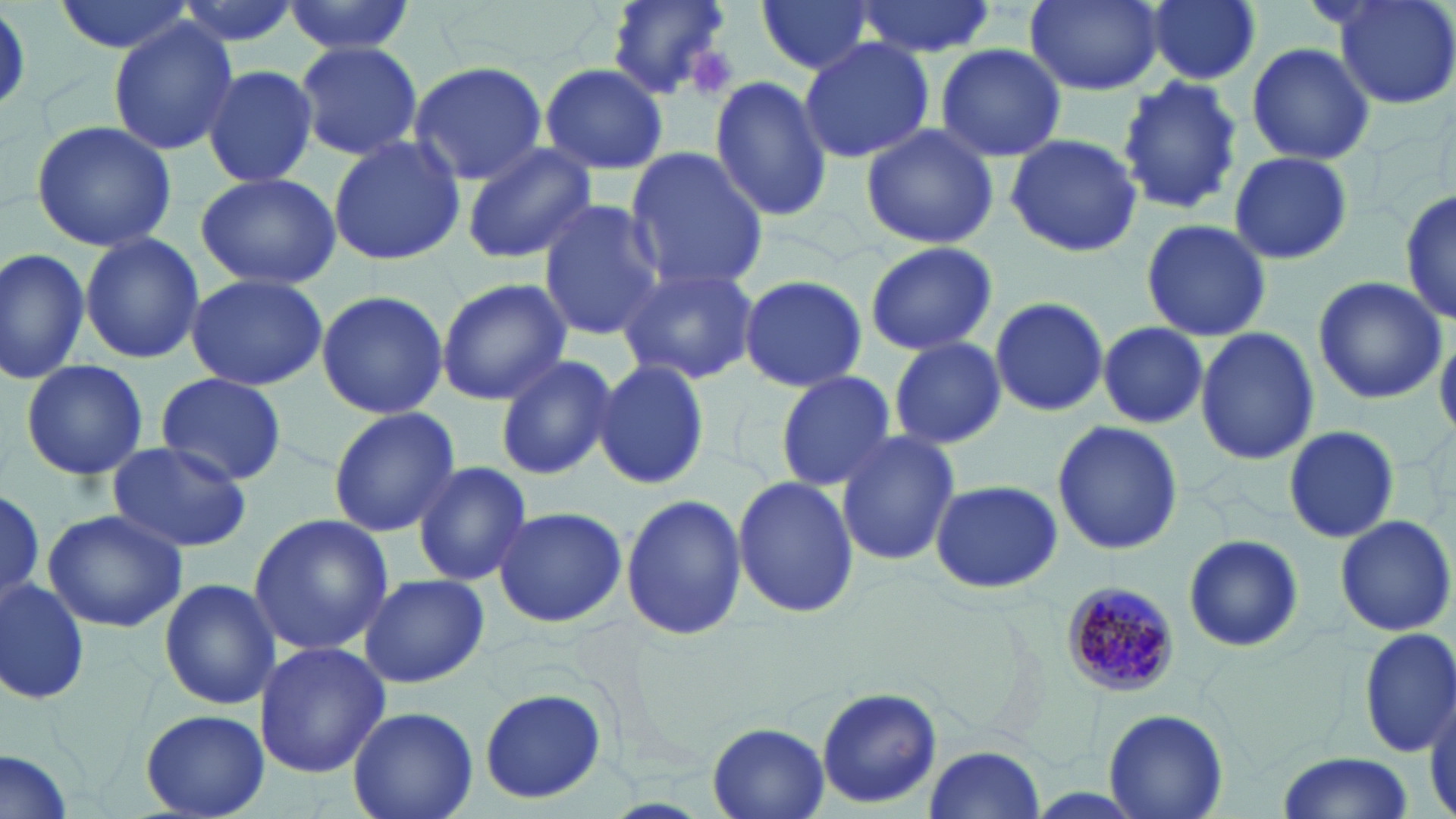

Approximate bounding boxes as (x1, y1, x2, y2) in pixels. Uninfected red blood cell locations: (52, 0, 198, 55), (169, 0, 304, 49), (285, 0, 415, 57), (605, 0, 735, 99), (755, 0, 871, 76), (1026, 0, 1163, 94), (1145, 0, 1262, 85), (1330, 0, 1456, 109), (850, 1, 995, 57), (108, 19, 237, 159), (797, 36, 935, 165), (293, 39, 424, 163), (1246, 41, 1376, 167), (935, 43, 1066, 164), (409, 60, 550, 185), (201, 63, 319, 189), (539, 63, 668, 175), (1117, 75, 1243, 218), (710, 76, 835, 221), (28, 120, 178, 252), (860, 123, 999, 248), (327, 133, 467, 267), (1003, 133, 1142, 258), (460, 142, 597, 265), (623, 148, 770, 293), (1227, 150, 1355, 263), (194, 171, 342, 289), (1400, 190, 1455, 326), (536, 199, 666, 340), (1139, 217, 1272, 342), (78, 232, 203, 363), (865, 241, 996, 354), (0, 247, 89, 384), (616, 264, 761, 386), (184, 273, 329, 391), (1311, 274, 1446, 406), (436, 275, 572, 406), (737, 275, 867, 392), (753, 275, 886, 485), (315, 289, 447, 421), (988, 296, 1108, 419), (1097, 322, 1209, 428), (1196, 326, 1319, 468), (1436, 327, 1456, 439), (888, 336, 1007, 449), (494, 353, 617, 480), (19, 358, 149, 483), (590, 358, 714, 489), (774, 370, 899, 492), (155, 371, 288, 486), (326, 407, 459, 538), (1051, 420, 1183, 555), (1282, 425, 1399, 543), (834, 430, 960, 567), (106, 441, 253, 553), (411, 463, 533, 586), (731, 476, 860, 618), (927, 477, 1061, 594), (0, 488, 45, 595), (620, 490, 747, 642), (492, 505, 629, 630), (42, 506, 189, 632), (247, 514, 392, 656), (1332, 514, 1456, 638), (1180, 533, 1303, 654), (356, 572, 490, 689), (1, 574, 91, 706), (158, 576, 281, 711), (1355, 625, 1456, 759), (254, 641, 389, 777), (477, 688, 609, 806), (817, 688, 941, 809), (348, 706, 477, 819), (140, 708, 269, 818), (1102, 708, 1229, 819), (706, 723, 829, 819), (922, 745, 1047, 818), (0, 750, 77, 819), (1274, 753, 1415, 819). Plasmodium malariae-infected red blood cell locations: (1064, 580, 1182, 695). Platelet locations: (683, 46, 736, 98). Slide-level diagnosis: Plasmodium malariae. Thin blood smear. One field of a larger specimen. Optical microscopy. 1000x magnification. Image is 1456×819 pixels. May-Grünwald-Giemsa-stained preparation.